Assess this cell for malaria.
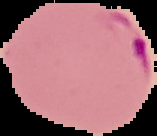

Parasitized.

image type = segmented cell region on a black background
preparation = thin blood film
image size = 157×136 pixels